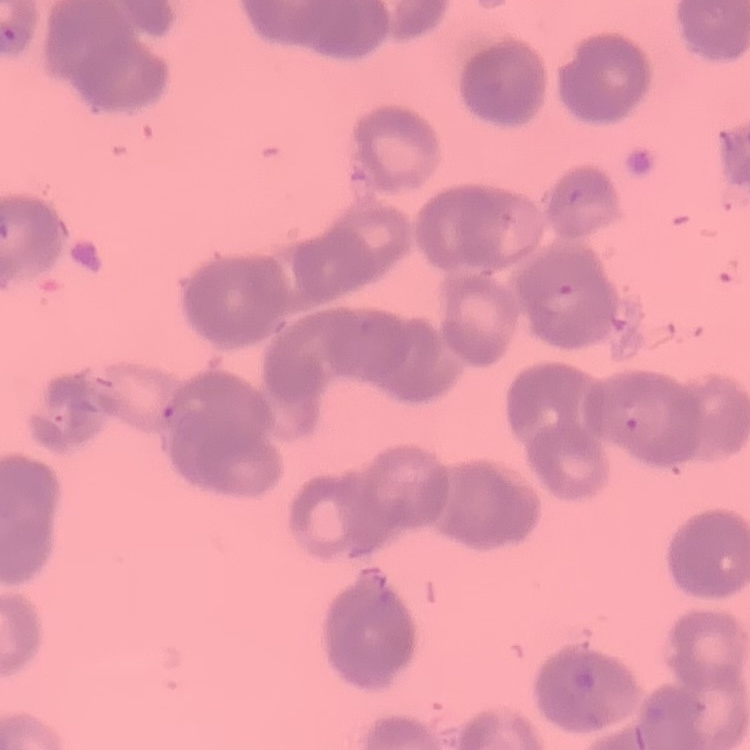

The red blood cells exhibit rouleaux formation. Stained with either Field's or Giemsa. Square crop of a larger photomicrograph. Thin peripheral smear.